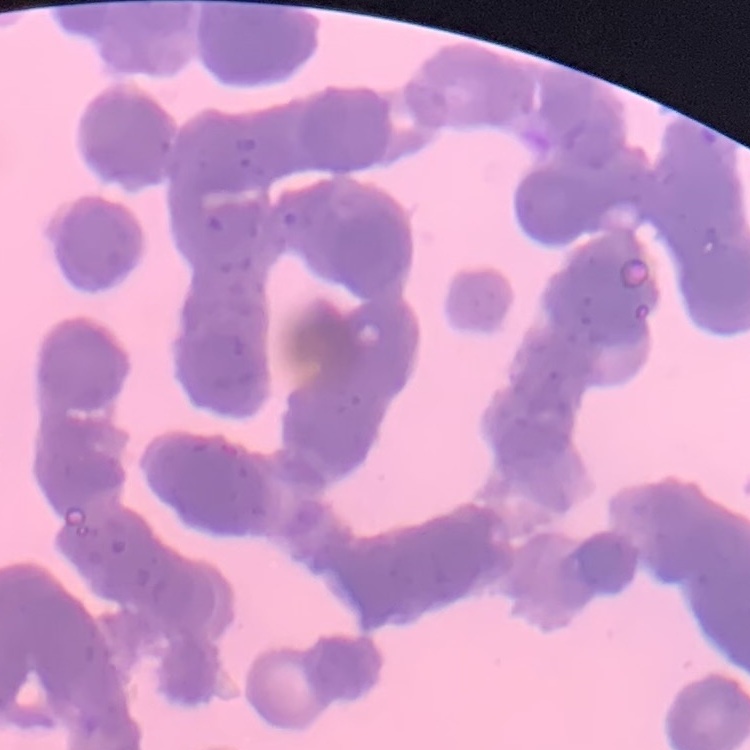
red_blood_cell_morphology: rouleaux formation
preparation: thin peripheral smear
image_type: square crop of a larger photomicrograph
stain: Field's or Giemsa